State the blood parasite species.
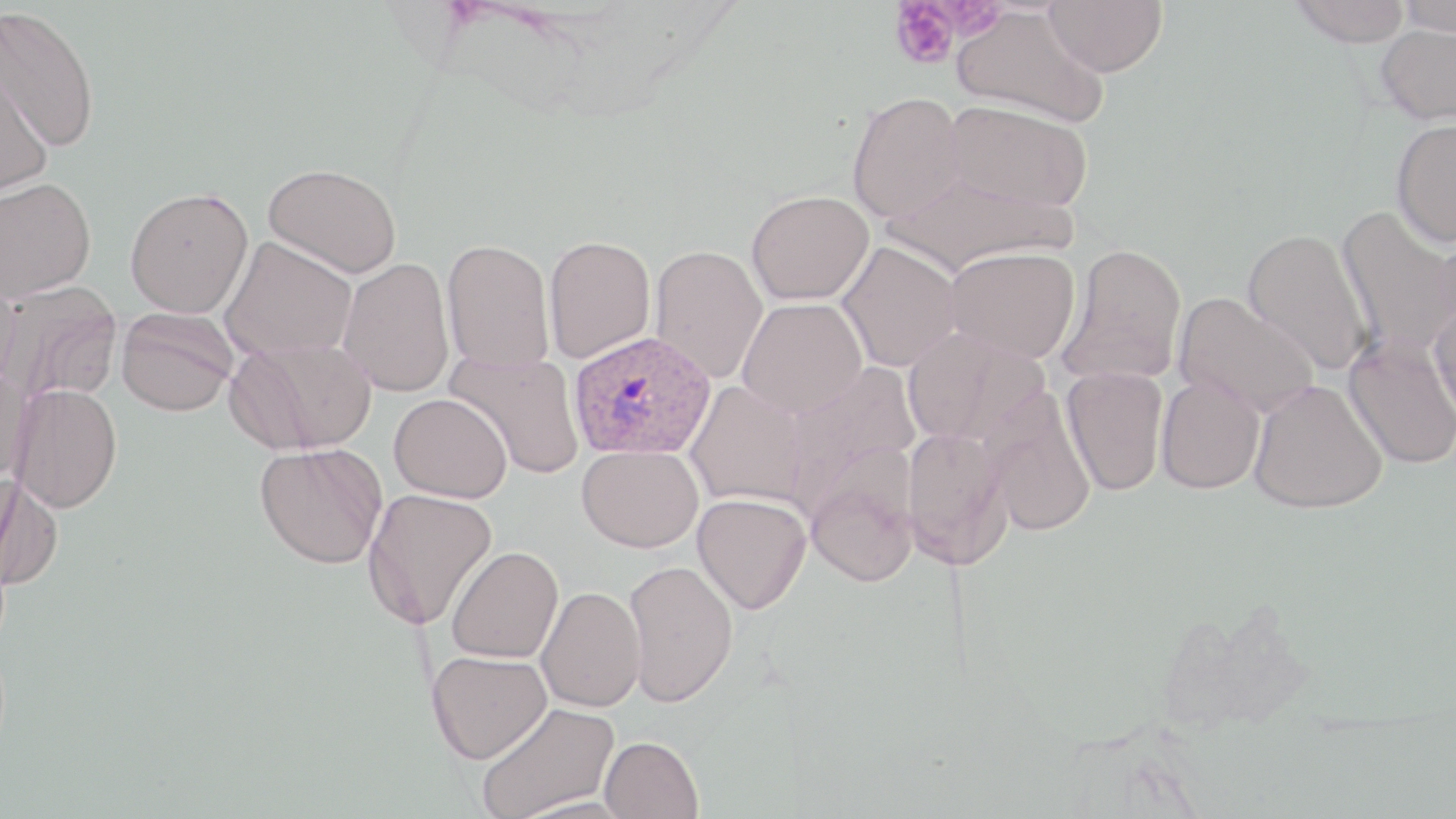
Plasmodium ovale.

Approximate bounding boxes as named x1/y1/x2/y2 corners in pixels. Plasmodium ovale-infected red blood cell locations: (x1=567, y1=330, x2=715, y2=461). Uninfected red blood cell locations: (x1=1044, y1=0, x2=1167, y2=77), (x1=1289, y1=0, x2=1412, y2=48), (x1=1397, y1=0, x2=1456, y2=37), (x1=0, y1=4, x2=103, y2=153), (x1=953, y1=7, x2=1109, y2=128), (x1=1375, y1=23, x2=1456, y2=125), (x1=0, y1=63, x2=53, y2=200), (x1=847, y1=91, x2=968, y2=223), (x1=943, y1=98, x2=1094, y2=213), (x1=1392, y1=118, x2=1456, y2=248), (x1=264, y1=162, x2=402, y2=279), (x1=881, y1=169, x2=1077, y2=276), (x1=0, y1=176, x2=96, y2=302), (x1=125, y1=186, x2=253, y2=318), (x1=746, y1=189, x2=874, y2=305), (x1=1336, y1=204, x2=1456, y2=360), (x1=1435, y1=209, x2=1456, y2=345), (x1=1243, y1=228, x2=1374, y2=376), (x1=543, y1=235, x2=656, y2=364), (x1=219, y1=236, x2=357, y2=361), (x1=441, y1=239, x2=554, y2=374), (x1=836, y1=241, x2=963, y2=372), (x1=1058, y1=243, x2=1187, y2=385), (x1=649, y1=244, x2=768, y2=383), (x1=945, y1=246, x2=1081, y2=364), (x1=338, y1=258, x2=455, y2=397), (x1=0, y1=274, x2=24, y2=394), (x1=2, y1=282, x2=121, y2=404), (x1=1173, y1=291, x2=1318, y2=418), (x1=737, y1=298, x2=867, y2=419), (x1=1428, y1=298, x2=1456, y2=431), (x1=116, y1=308, x2=239, y2=417), (x1=902, y1=327, x2=1049, y2=446), (x1=1344, y1=335, x2=1456, y2=470), (x1=228, y1=336, x2=377, y2=454), (x1=447, y1=350, x2=586, y2=481), (x1=779, y1=363, x2=920, y2=514), (x1=1062, y1=366, x2=1168, y2=495), (x1=0, y1=369, x2=33, y2=484), (x1=1156, y1=375, x2=1265, y2=494), (x1=1249, y1=379, x2=1387, y2=514), (x1=684, y1=381, x2=808, y2=508), (x1=11, y1=384, x2=122, y2=512), (x1=981, y1=388, x2=1096, y2=537), (x1=389, y1=392, x2=513, y2=503), (x1=901, y1=426, x2=1012, y2=568), (x1=256, y1=442, x2=388, y2=569), (x1=577, y1=444, x2=704, y2=553), (x1=805, y1=465, x2=920, y2=587), (x1=0, y1=475, x2=63, y2=591), (x1=362, y1=488, x2=499, y2=629), (x1=693, y1=493, x2=811, y2=614), (x1=446, y1=545, x2=563, y2=664), (x1=623, y1=560, x2=739, y2=706), (x1=536, y1=586, x2=645, y2=712), (x1=427, y1=650, x2=551, y2=763), (x1=476, y1=701, x2=619, y2=819), (x1=600, y1=735, x2=704, y2=819), (x1=508, y1=796, x2=637, y2=818). Platelet locations: (x1=890, y1=2, x2=961, y2=70). Thin blood smear. One field of a larger specimen. Light microscopy. Image is 1456×819 pixels. May-Grünwald-Giemsa-stained preparation. 1000x magnification.